Classify this cell by malaria status.
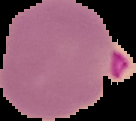
It is parasitized.

From a thin blood film. Image is 136×121 pixels. Segmented cell region on a black background.